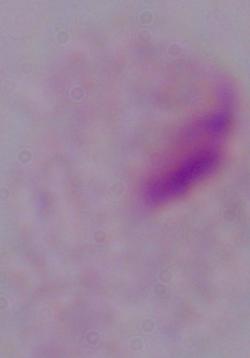

magnification = 1000x
modality = micrograph
identification = trichomonad